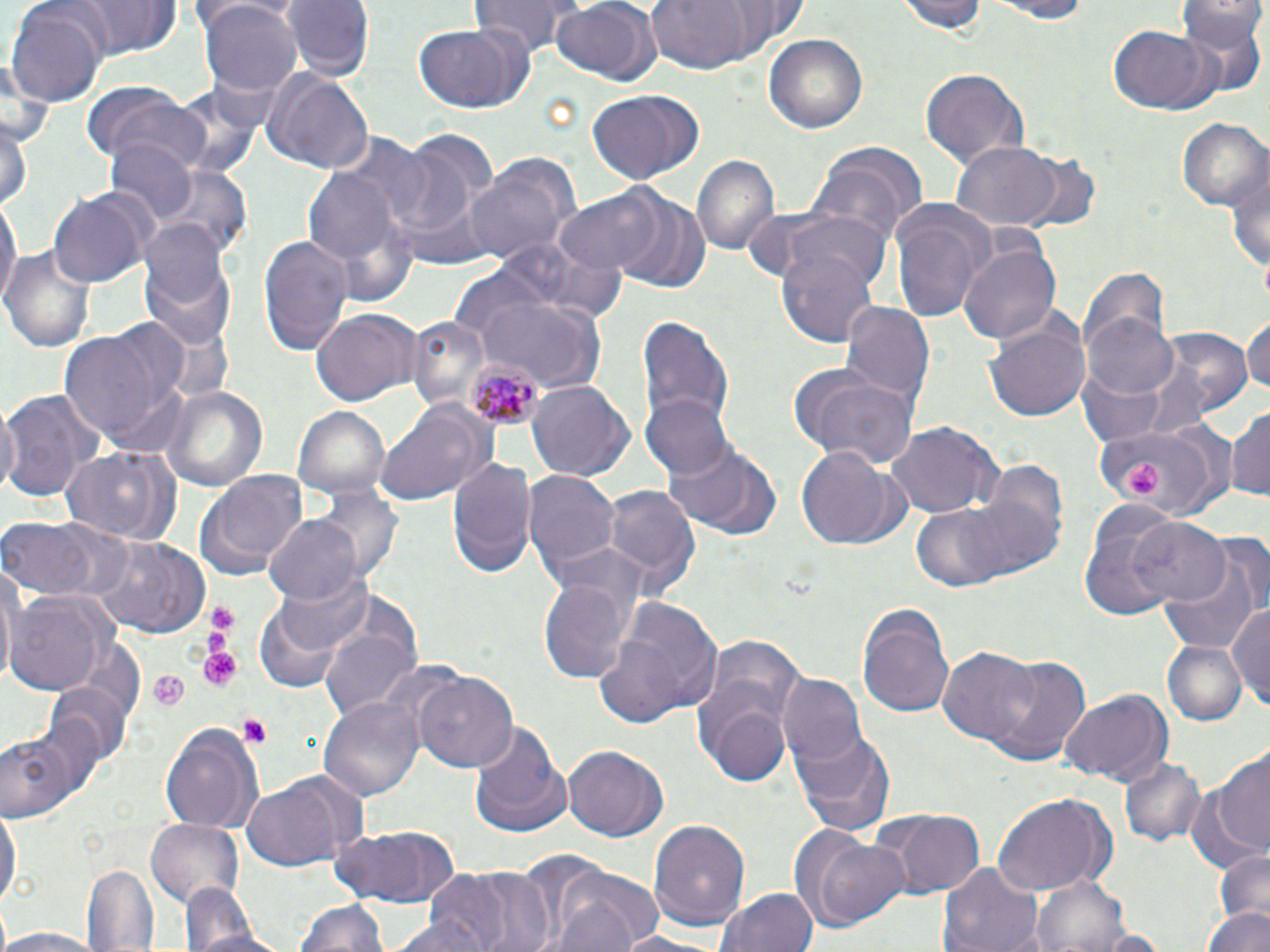
Summary:
  - Coordinate format: approximate bounding boxes as (x1, y1, x2, y2) in pixels
  - Platelet locations: (1123, 458, 1164, 501), (202, 602, 241, 653), (196, 647, 244, 691), (146, 669, 188, 713), (236, 712, 270, 747)
  - Uninfected red blood cell locations: (63, 0, 187, 60), (283, 0, 370, 80), (473, 0, 582, 52), (642, 0, 764, 76), (896, 0, 991, 36), (977, 0, 1097, 21), (550, 1, 661, 87), (1177, 1, 1267, 98), (200, 4, 299, 95), (7, 7, 106, 106), (1108, 23, 1217, 115), (412, 26, 526, 112), (765, 33, 868, 133), (260, 65, 374, 175), (920, 68, 1028, 168), (86, 87, 210, 174), (585, 91, 697, 185), (1, 116, 32, 217), (1178, 117, 1270, 214), (104, 139, 199, 229), (950, 141, 1063, 230), (806, 143, 926, 248), (1224, 148, 1270, 282), (691, 154, 780, 257), (1014, 155, 1101, 235), (465, 160, 573, 271), (305, 166, 401, 268), (154, 168, 253, 263), (556, 190, 663, 277), (1, 191, 19, 313), (50, 192, 145, 289), (612, 192, 711, 297), (887, 199, 998, 322), (741, 203, 888, 288), (137, 215, 233, 328), (502, 232, 626, 329), (259, 233, 353, 355), (776, 242, 881, 349), (959, 244, 1060, 345), (2, 245, 96, 349), (1078, 266, 1169, 360), (459, 280, 608, 391), (841, 301, 937, 409), (311, 310, 420, 406), (1084, 310, 1184, 403), (984, 312, 1092, 423), (635, 314, 736, 440), (1242, 316, 1270, 400), (404, 318, 488, 410), (1150, 328, 1253, 426), (58, 329, 173, 446), (785, 362, 918, 470), (1073, 367, 1168, 449), (526, 379, 633, 480), (162, 386, 267, 492), (1, 387, 106, 504), (643, 394, 734, 480), (375, 399, 496, 507), (1228, 405, 1270, 503), (293, 407, 390, 502), (887, 420, 1000, 521), (1089, 421, 1221, 511), (662, 438, 782, 540), (60, 445, 180, 546), (797, 448, 898, 550), (447, 457, 536, 579), (194, 469, 308, 583), (524, 469, 620, 587), (317, 484, 400, 580), (599, 484, 701, 595), (904, 496, 1042, 594), (1077, 504, 1188, 617), (263, 514, 360, 604), (2, 518, 98, 600), (1129, 518, 1230, 609), (96, 536, 210, 641), (1157, 541, 1265, 656), (1, 566, 18, 691), (272, 569, 378, 660), (539, 573, 634, 687), (5, 594, 106, 699), (597, 594, 724, 727), (1228, 599, 1270, 704), (857, 601, 957, 717), (321, 623, 422, 720), (695, 632, 810, 766), (1163, 643, 1246, 723), (938, 648, 1042, 747), (982, 653, 1091, 767), (414, 672, 519, 776), (777, 675, 866, 768), (43, 683, 134, 773), (1061, 689, 1176, 784), (697, 693, 794, 787), (320, 694, 423, 799), (160, 722, 265, 832), (469, 722, 569, 834), (789, 724, 896, 837), (2, 730, 74, 821), (563, 746, 669, 842), (1214, 749, 1270, 857), (1120, 757, 1207, 850), (1182, 773, 1265, 872), (240, 776, 360, 872), (991, 792, 1115, 893), (0, 803, 20, 915), (881, 809, 985, 897), (148, 819, 245, 907), (648, 819, 751, 930), (327, 824, 460, 908), (814, 838, 914, 929), (514, 849, 611, 948), (1210, 849, 1270, 925), (938, 862, 1044, 952), (85, 863, 159, 951), (446, 865, 558, 952), (545, 866, 665, 951), (1031, 875, 1134, 952), (178, 881, 272, 952), (720, 886, 819, 952), (294, 896, 389, 952), (1204, 905, 1269, 952), (390, 913, 493, 952), (1082, 926, 1172, 951), (0, 927, 103, 952), (606, 930, 718, 951)
  - Plasmodium malariae-infected red blood cell locations: (465, 358, 545, 429)
  - Slide-level diagnosis: Plasmodium malariae
  - Magnification: 1000x
  - Field of view: one of a larger specimen
  - Stain: May-Grünwald-Giemsa
  - Modality: optical microscopy
  - Preparation: thin blood film
  - Image size: 1270×952 pixels